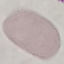
{
  "result": "no malaria parasites detected",
  "image_type": "automatically extracted cell patch, resized to 64 × 64 pixels",
  "capture": "smartphone through the microscope eyepiece",
  "stain": "Giemsa",
  "preparation": "thin smear"
}